Assess this cell for malaria.
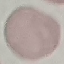

It is uninfected.

Giemsa-stained preparation. Cell patch, automatically extracted from a larger field of view and resized to 64 × 64 pixels. Thin smear of blood. Acquired by smartphone through the microscope eyepiece.